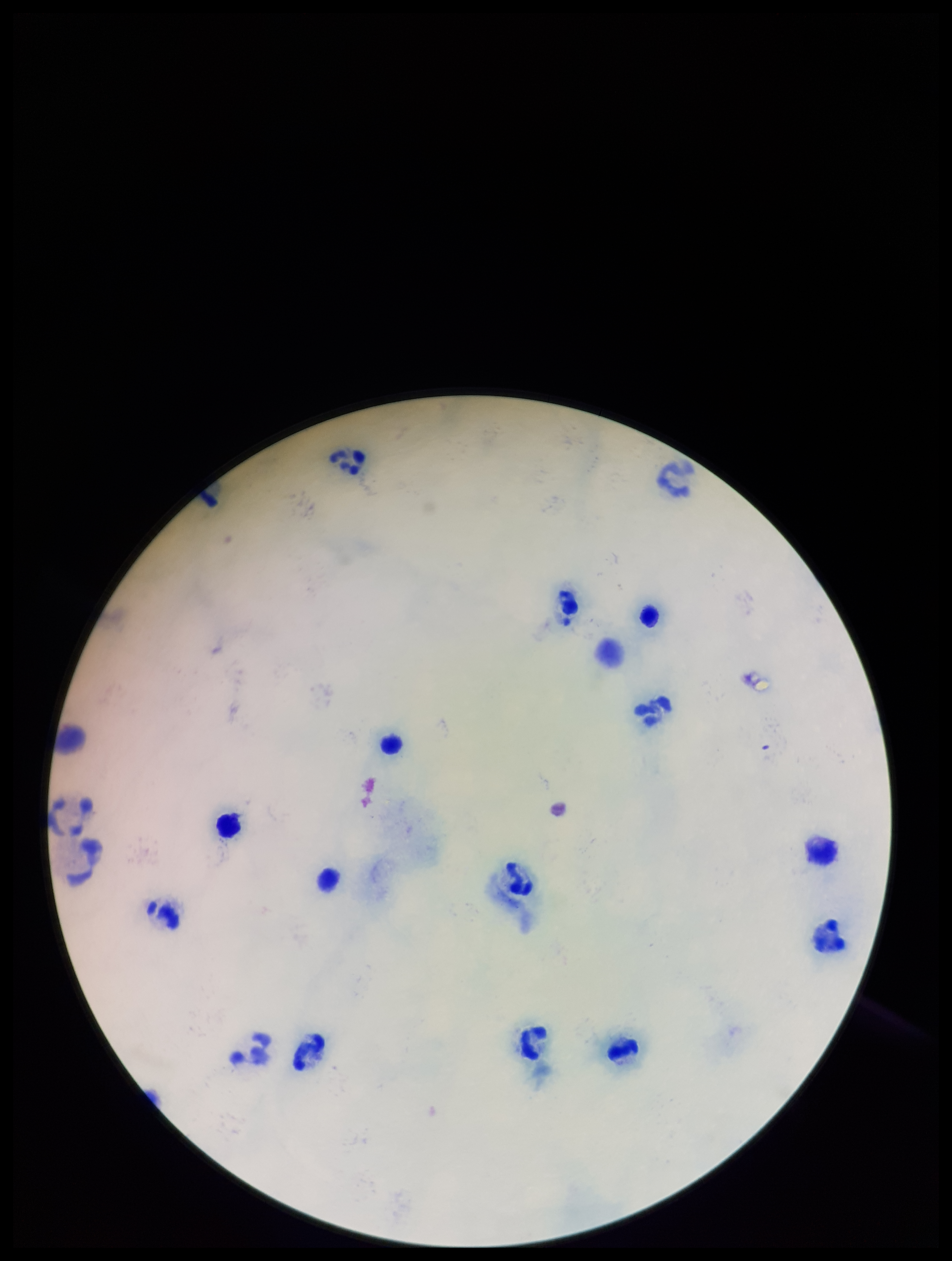
Summary:
  - Plasmodium parasites: none detected
  - Image size: 952×1261 pixels
  - Patient malaria status: negative
  - Stain: Giemsa
  - Leukocyte count: 17
  - Parasite count: 0
  - Capture: smartphone photograph through the microscope eyepiece
  - Preparation: thick smear
  - Field of view: one from this slide